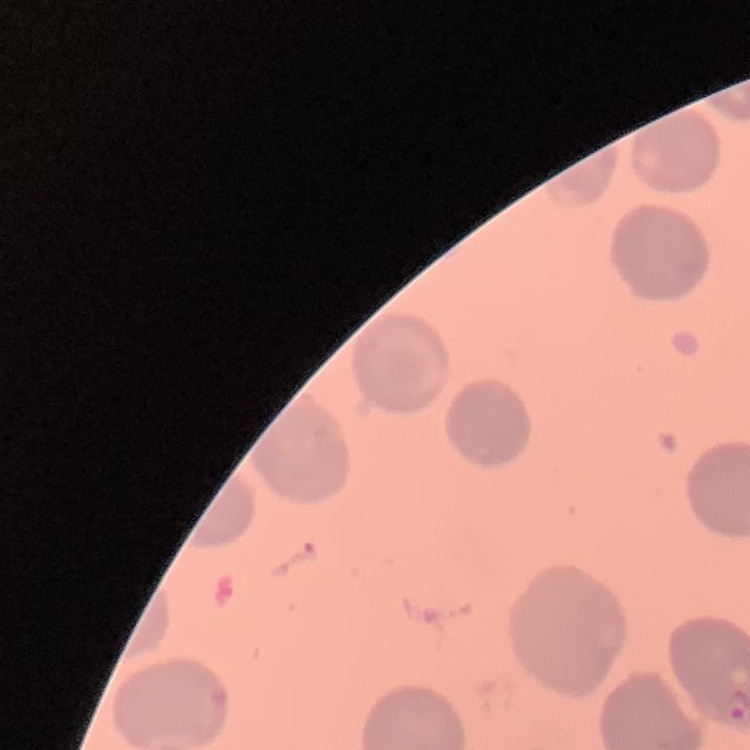

erythrocyte morphology = no rouleaux formation
stain = Field's or Giemsa
preparation = thin peripheral smear
image type = square crop of a larger photomicrograph